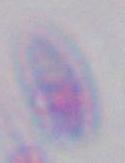
Micrograph. Toxoplasma gondii is seen. 1000x magnification.